Give the extent of all Trypanosoma brucei.
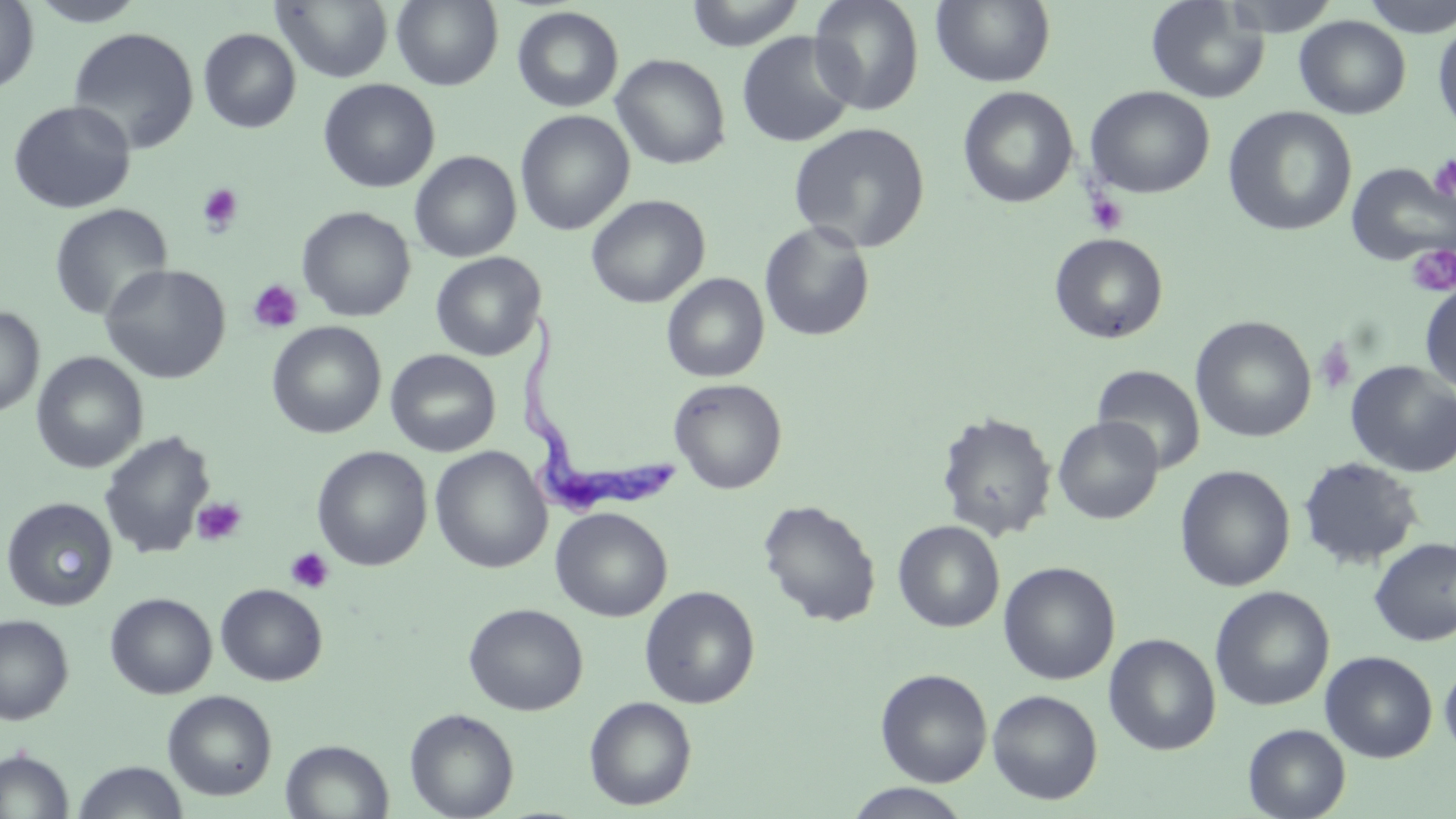
Approximate bounding boxes as [x1, y1, x2, y2] in pixels.
Trypanosoma brucei: [521, 312, 676, 524].

Uninfected red blood cell locations: [0, 0, 39, 95], [26, 0, 149, 26], [273, 0, 394, 83], [391, 0, 504, 90], [682, 0, 807, 50], [808, 0, 926, 115], [930, 0, 1056, 88], [1145, 0, 1269, 104], [1221, 0, 1344, 36], [1358, 0, 1456, 38], [512, 6, 624, 112], [1294, 16, 1411, 119], [1432, 20, 1456, 138], [67, 26, 200, 154], [198, 28, 302, 134], [736, 31, 858, 148], [610, 53, 731, 170], [318, 79, 440, 193], [1084, 85, 1215, 199], [957, 86, 1079, 209], [8, 100, 136, 214], [1222, 106, 1357, 236], [515, 110, 635, 235], [787, 121, 931, 254], [409, 151, 522, 262], [1345, 161, 1456, 267], [586, 194, 710, 308], [49, 203, 172, 321], [297, 207, 416, 322], [758, 221, 875, 342], [1049, 233, 1168, 344], [430, 252, 545, 361], [99, 264, 231, 384], [661, 273, 769, 382], [1419, 282, 1456, 394], [0, 306, 44, 417], [1190, 316, 1316, 443], [266, 321, 386, 439], [385, 349, 501, 457], [32, 353, 149, 474], [1345, 361, 1456, 477], [1092, 365, 1206, 473], [668, 378, 787, 494], [935, 411, 1057, 542], [1053, 416, 1163, 524], [99, 430, 216, 560], [312, 446, 432, 571], [429, 446, 552, 573], [1297, 457, 1423, 570], [1174, 464, 1295, 592], [2, 497, 117, 611], [758, 499, 881, 627], [550, 507, 673, 622], [893, 520, 1005, 632], [1368, 536, 1456, 646], [998, 561, 1120, 685], [215, 583, 327, 686], [1209, 585, 1334, 711], [639, 586, 760, 709], [105, 592, 217, 699], [463, 602, 588, 716], [0, 615, 74, 725], [1103, 633, 1221, 755], [1320, 651, 1437, 762], [1440, 660, 1456, 761], [875, 668, 992, 786], [162, 689, 278, 801], [987, 689, 1103, 804], [584, 696, 696, 810], [405, 708, 519, 819], [1243, 724, 1350, 819], [280, 739, 394, 819], [0, 749, 74, 818], [72, 761, 189, 819], [842, 784, 974, 819]. Platelet locations: [1428, 154, 1456, 203], [196, 183, 244, 235], [1084, 190, 1129, 236], [1406, 245, 1456, 298], [248, 280, 303, 334], [1314, 339, 1357, 395], [191, 497, 247, 546], [284, 547, 334, 594]. Slide-level diagnosis: Trypanosoma brucei. Image is 1456×819 pixels. Thin blood smear. One field of a larger specimen. Light microscopy. 1000x magnification. May-Grünwald-Giemsa stain.